Point out leukocytes.
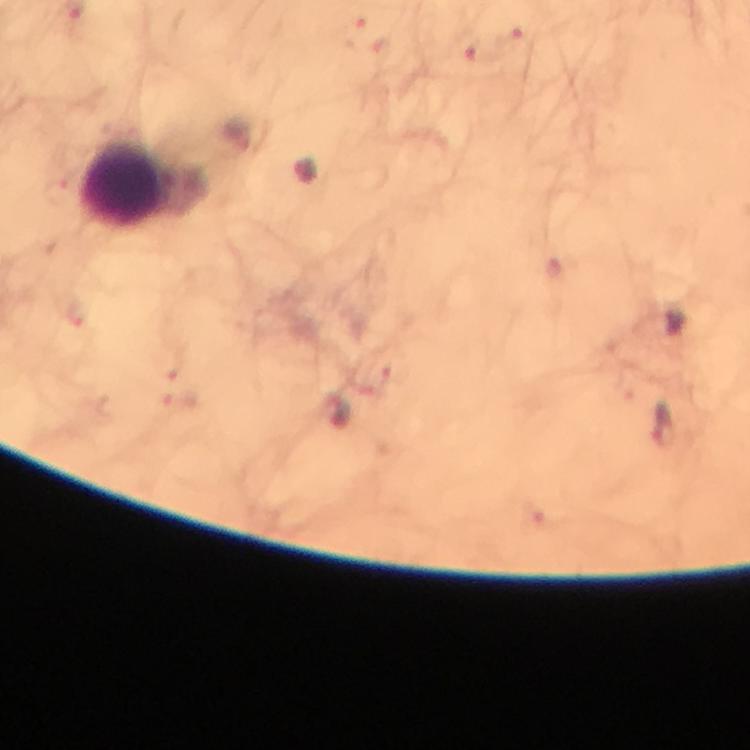

Approximate object centers, in pixels from the top-left corner.
Leukocytes: (x=126, y=184).

Plasmodium parasite locations: (x=354, y=29), (x=515, y=41), (x=380, y=50), (x=479, y=56), (x=666, y=425). Cropped region of a single field of view. Smartphone photograph taken through a microscope. Immersion oil was used. 100x magnification. Image is 750×750 pixels. Thick smear. From a diagnostic examination for malaria. Giemsa stain.